Classify this cell by malaria status.
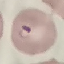
Parasitized.

Summary:
  - Capture: smartphone through the microscope eyepiece
  - Image type: automatically extracted cell patch, resized to 64 × 64 pixels
  - Preparation: thin blood smear
  - Stain: Giemsa